Identify the parasite.
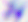
This is Toxoplasma gondii.

Summary:
  - Magnification: 400x
  - Modality: micrograph